Classify this cell by malaria status.
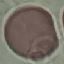
It is uninfected.

Thin blood film. Giemsa-stained preparation. Cell patch, automatically extracted from a larger field of view and resized to 64 × 64 pixels. Photographed with a smartphone camera at the microscope eyepiece.